Identify the cell.
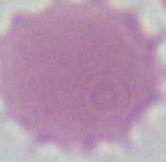

This is an erythrocyte.

Summary:
  - Modality: micrograph
  - Magnification: 1000x